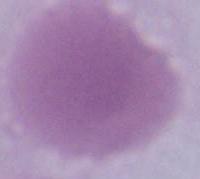

A red blood cell is seen. 1000x magnification. Micrograph.